State the preparation type.
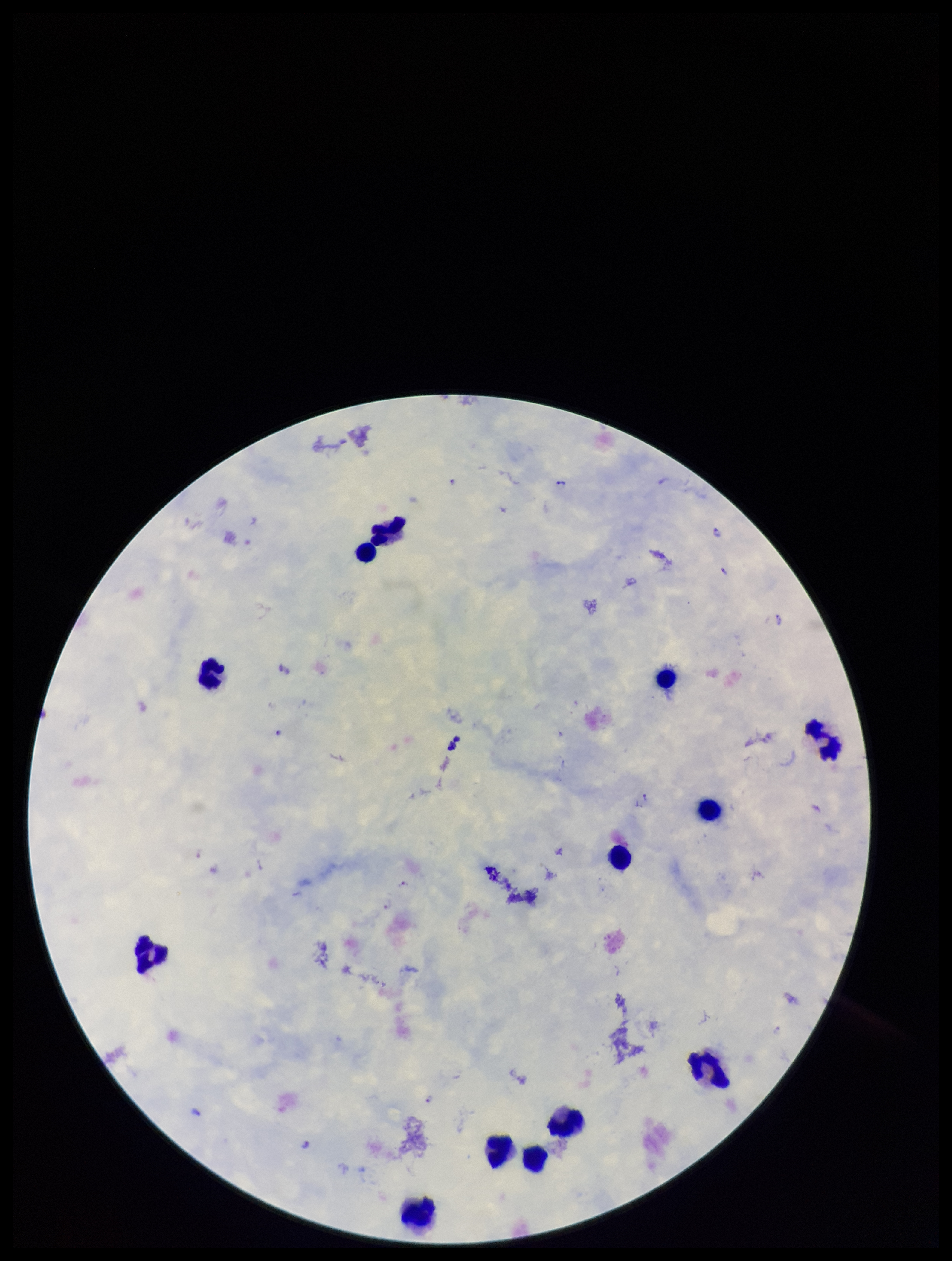

A thick smear.

Plasmodium parasites = identified
leukocyte count = 13
stain = Giemsa
patient malaria status = positive
field of view = single
capture = smartphone photograph through the microscope eyepiece
species reported for this patient = Plasmodium falciparum
parasite count = 10
image size = 952×1261 pixels